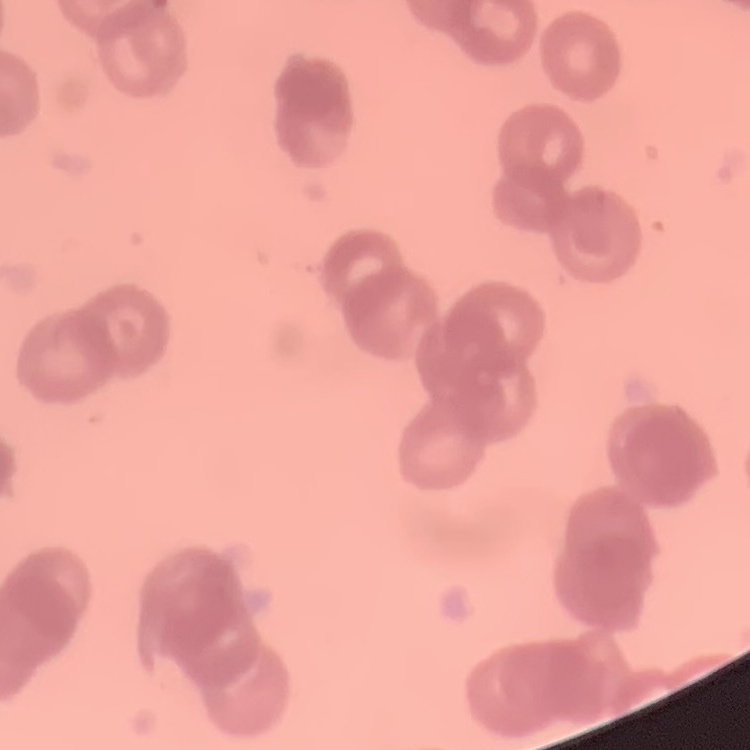

erythrocyte morphology = rouleaux formation
stain = Field's or Giemsa
preparation = thin blood film
image type = square crop of a larger photomicrograph